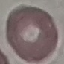
Result: negative for malaria parasites. Photographed with a smartphone camera at the microscope eyepiece. Automatically extracted cell patch, resized to 64 × 64 pixels. Giemsa stain. Thin smear of blood.